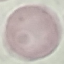 Malaria status: uninfected. Automatically extracted cell patch, resized to 64 × 64 pixels. Giemsa-stained preparation. Acquired by smartphone through the microscope eyepiece. Thin blood film.